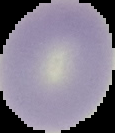
preparation = thin blood film
image type = cell region segmented out of the field of view; surrounding area masked to black
malaria status = uninfected
image size = 115×133 pixels